State the blood parasite species.
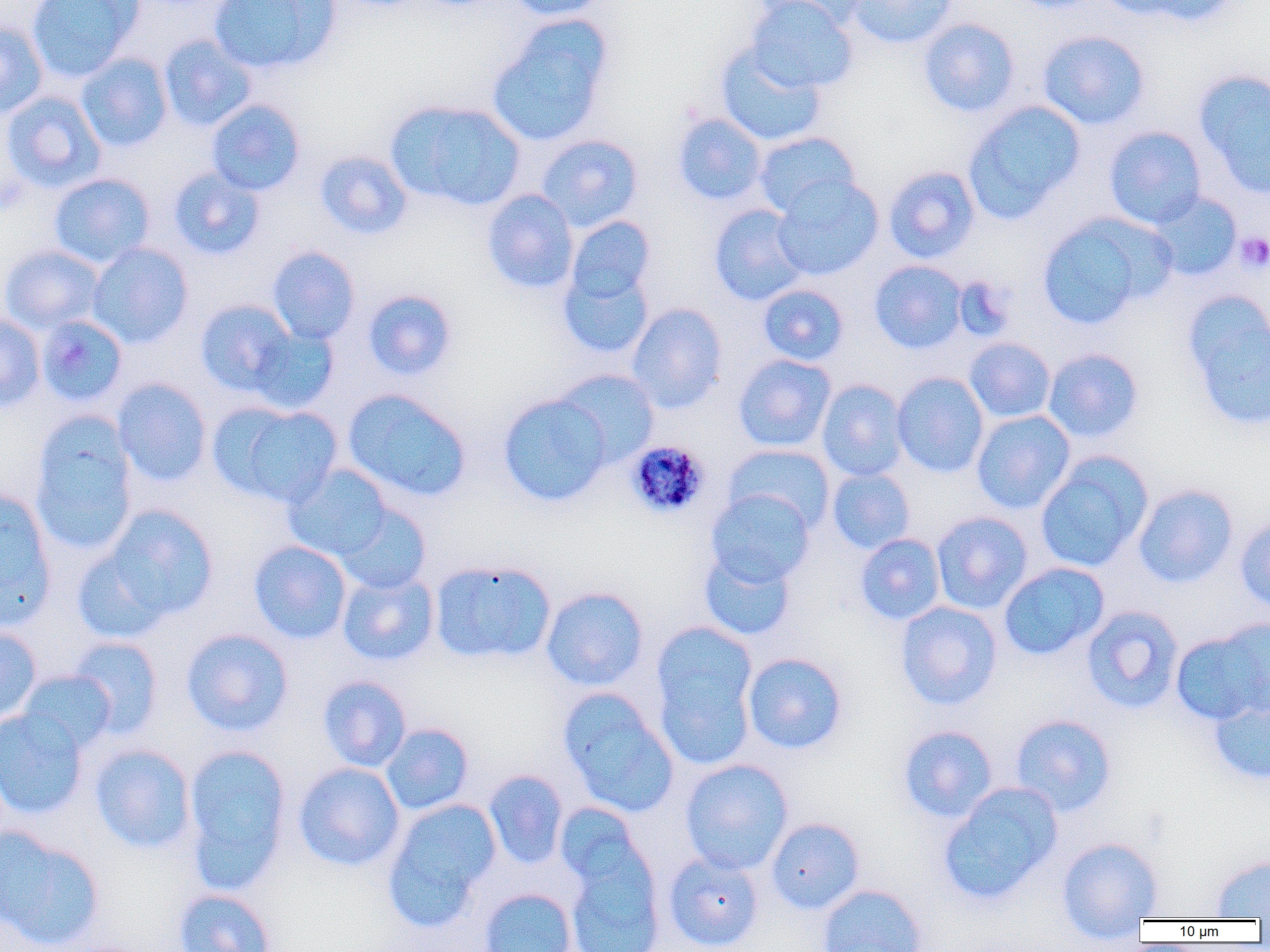

Plasmodium malariae.

platelet locations = approximate bounding boxes as [x1, y1, x2, y2] in pixels: [1235, 232, 1270, 273]
magnification = 1000x
image size = 1270×952 pixels
Plasmodium malariae-infected red blood cell locations = approximate bounding boxes as [x1, y1, x2, y2] in pixels: [625, 441, 711, 519]
uninfected red blood cell locations = approximate bounding boxes as [x1, y1, x2, y2] in pixels: [26, 0, 143, 82], [209, 0, 340, 74], [506, 0, 609, 20], [746, 0, 858, 93], [749, 0, 867, 29], [845, 0, 959, 49], [1000, 0, 1106, 12], [1096, 0, 1199, 22], [1133, 0, 1242, 27], [487, 17, 613, 146], [917, 18, 1021, 117], [0, 21, 47, 119], [1037, 29, 1150, 130], [158, 34, 257, 132], [715, 43, 827, 147], [76, 53, 173, 152], [1193, 69, 1270, 197], [2, 91, 106, 193], [206, 99, 306, 196], [387, 99, 525, 212], [963, 100, 1086, 224], [672, 112, 768, 206], [1104, 126, 1207, 229], [753, 131, 859, 218], [536, 134, 643, 231], [314, 150, 413, 240], [883, 165, 981, 263], [168, 166, 265, 260], [49, 173, 156, 269], [772, 175, 884, 281], [481, 189, 579, 294], [1147, 191, 1242, 281], [709, 204, 809, 306], [1035, 213, 1169, 330], [565, 215, 655, 306], [86, 242, 194, 348], [1, 244, 105, 334], [266, 246, 360, 344], [869, 260, 967, 354], [558, 265, 654, 359], [758, 283, 849, 366], [361, 289, 458, 381], [1182, 292, 1270, 431], [195, 299, 296, 396], [626, 303, 727, 413], [0, 313, 46, 413], [36, 315, 129, 408], [248, 326, 339, 414], [964, 337, 1057, 423], [1043, 348, 1144, 443], [733, 354, 836, 452], [553, 368, 659, 467], [892, 371, 990, 478], [113, 378, 212, 486], [816, 379, 909, 481], [342, 389, 472, 503], [497, 392, 613, 506], [209, 401, 344, 508], [971, 410, 1075, 514], [29, 413, 138, 555], [724, 443, 835, 533], [1034, 452, 1153, 573], [282, 464, 394, 563], [827, 467, 915, 554], [1133, 483, 1238, 588], [0, 486, 57, 631], [706, 489, 815, 585], [334, 502, 432, 594], [96, 504, 219, 626], [931, 511, 1033, 614], [1234, 517, 1270, 613], [855, 533, 946, 625], [249, 540, 352, 644], [699, 546, 797, 641], [429, 559, 556, 665], [998, 562, 1109, 660], [337, 570, 439, 667], [540, 586, 649, 691], [896, 601, 1002, 710], [1082, 605, 1184, 715], [651, 621, 758, 760], [1171, 624, 1269, 726], [0, 626, 42, 724], [181, 628, 294, 737], [67, 636, 164, 739], [742, 652, 848, 754], [17, 669, 117, 753], [318, 675, 412, 772], [559, 689, 678, 817], [1208, 695, 1270, 785], [0, 707, 89, 820], [1010, 714, 1117, 816], [380, 722, 474, 815], [897, 725, 999, 822], [90, 743, 197, 853], [182, 743, 292, 892], [680, 758, 794, 874], [293, 762, 405, 871], [484, 769, 568, 869], [938, 783, 1062, 904], [382, 797, 501, 929], [554, 803, 649, 895], [766, 817, 865, 914], [0, 826, 105, 949], [1057, 837, 1164, 928], [564, 849, 665, 952], [662, 851, 765, 951], [1210, 854, 1270, 919], [815, 883, 928, 952], [478, 887, 578, 952], [173, 888, 276, 952]
preparation = thin blood film
modality = optical microscopy
field of view = single